Assess this cell for malaria.
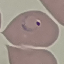

Parasitized.

Cell patch, automatically extracted from a larger field of view and resized to 64 × 64 pixels. Thin blood smear. Photographed with a smartphone camera at the microscope eyepiece. Giemsa stain.